Assess this cell for malaria.
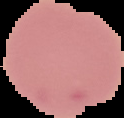

It is uninfected.

image size = 124×118 pixels
image type = segmented cell region with the area outside set to black
preparation = thin blood film